Assess this cell for malaria.
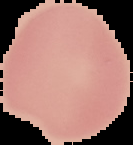
It is uninfected.

image size = 133×145 pixels
preparation = thin blood film
image type = segmented cell region on a black background